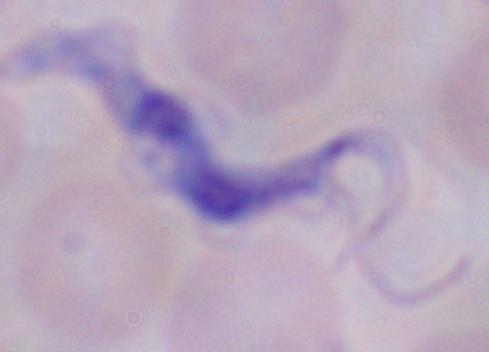

Summary:
  - Identification: trypanosome
  - Modality: micrograph
  - Magnification: 1000x